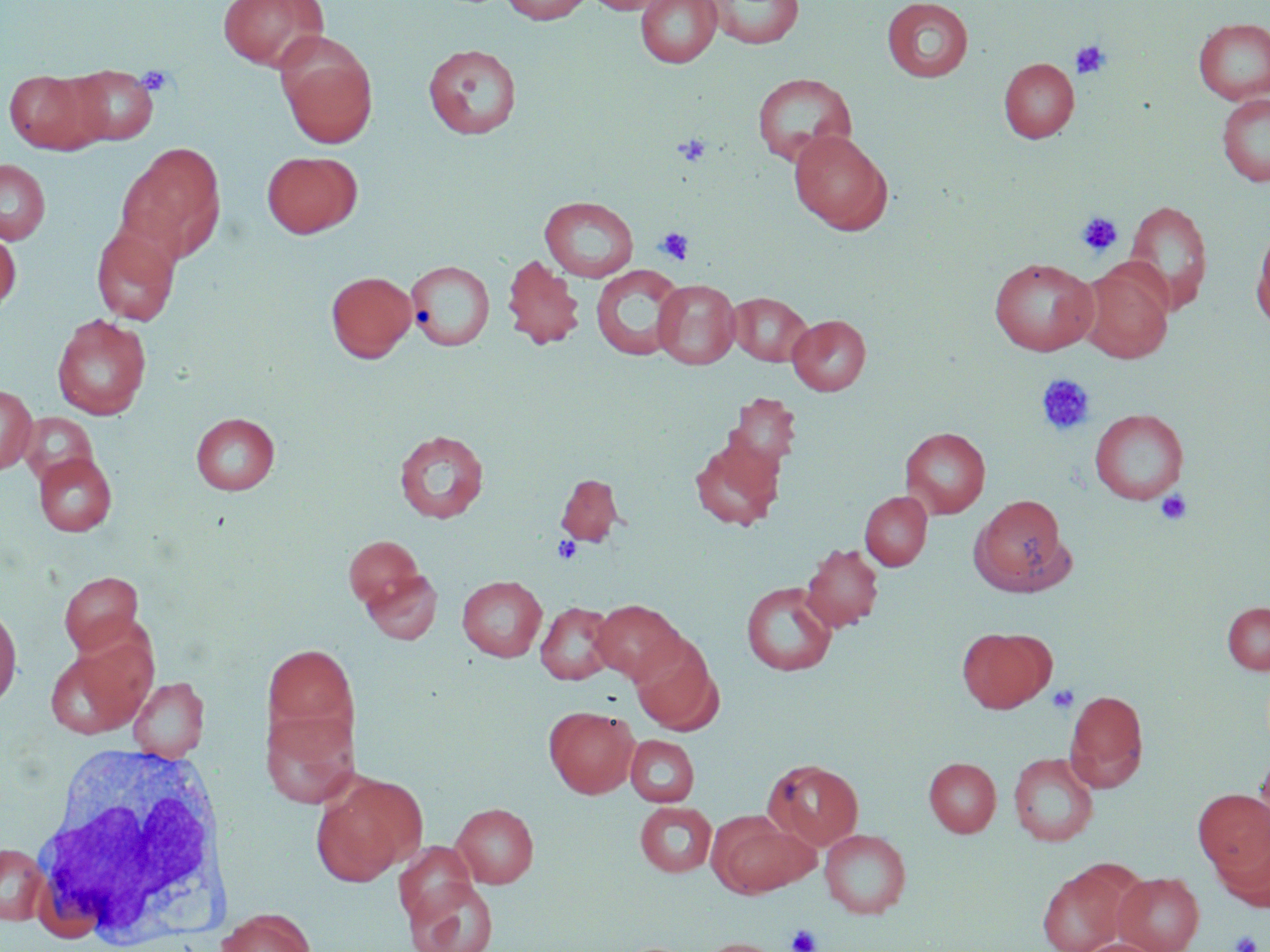
slide-level diagnosis = negative for blood parasites
image size = 1270×952 pixels
modality = light microscopy
platelet locations = approximate bounding boxes as named x1/y1/x2/y2 corners in pixels: (x1=1070, y1=40, x2=1112, y2=80), (x1=137, y1=65, x2=177, y2=97), (x1=673, y1=134, x2=711, y2=166), (x1=1076, y1=211, x2=1123, y2=257), (x1=655, y1=226, x2=694, y2=266), (x1=1036, y1=374, x2=1096, y2=436), (x1=1155, y1=490, x2=1193, y2=525), (x1=552, y1=536, x2=582, y2=564), (x1=1047, y1=684, x2=1079, y2=713), (x1=786, y1=924, x2=822, y2=952), (x1=1230, y1=931, x2=1262, y2=952)
stain = May-Grünwald-Giemsa
white blood cell locations = approximate bounding boxes as named x1/y1/x2/y2 corners in pixels: (x1=24, y1=743, x2=230, y2=951)
preparation = thin blood film
uninfected red blood cell locations = approximate bounding boxes as named x1/y1/x2/y2 corners in pixels: (x1=217, y1=0, x2=328, y2=72), (x1=500, y1=0, x2=592, y2=25), (x1=586, y1=0, x2=671, y2=14), (x1=635, y1=0, x2=722, y2=68), (x1=703, y1=0, x2=804, y2=49), (x1=881, y1=0, x2=973, y2=82), (x1=1193, y1=17, x2=1270, y2=105), (x1=275, y1=36, x2=378, y2=150), (x1=423, y1=43, x2=522, y2=139), (x1=999, y1=57, x2=1079, y2=143), (x1=63, y1=64, x2=160, y2=144), (x1=4, y1=69, x2=106, y2=154), (x1=751, y1=72, x2=858, y2=168), (x1=1216, y1=93, x2=1270, y2=187), (x1=789, y1=129, x2=893, y2=233), (x1=115, y1=141, x2=226, y2=264), (x1=262, y1=150, x2=362, y2=238), (x1=0, y1=158, x2=51, y2=244), (x1=540, y1=196, x2=639, y2=282), (x1=1123, y1=199, x2=1213, y2=313), (x1=1251, y1=222, x2=1270, y2=332), (x1=91, y1=225, x2=181, y2=326), (x1=0, y1=228, x2=21, y2=315), (x1=502, y1=254, x2=585, y2=350), (x1=989, y1=257, x2=1098, y2=356), (x1=405, y1=259, x2=494, y2=352), (x1=1078, y1=262, x2=1174, y2=362), (x1=590, y1=264, x2=686, y2=360), (x1=326, y1=270, x2=417, y2=362), (x1=652, y1=278, x2=740, y2=369), (x1=727, y1=292, x2=813, y2=366), (x1=51, y1=314, x2=152, y2=420), (x1=788, y1=314, x2=871, y2=395), (x1=0, y1=384, x2=37, y2=473), (x1=725, y1=393, x2=802, y2=474), (x1=1089, y1=408, x2=1189, y2=505), (x1=191, y1=412, x2=280, y2=495), (x1=20, y1=413, x2=97, y2=487), (x1=900, y1=426, x2=991, y2=517), (x1=394, y1=429, x2=489, y2=523), (x1=689, y1=436, x2=784, y2=531), (x1=34, y1=452, x2=118, y2=536), (x1=555, y1=473, x2=624, y2=546), (x1=860, y1=491, x2=932, y2=571), (x1=971, y1=494, x2=1072, y2=595), (x1=343, y1=535, x2=427, y2=612), (x1=801, y1=544, x2=884, y2=632), (x1=360, y1=566, x2=442, y2=645), (x1=59, y1=571, x2=144, y2=656), (x1=457, y1=575, x2=547, y2=661), (x1=741, y1=580, x2=837, y2=676), (x1=591, y1=599, x2=686, y2=684), (x1=0, y1=601, x2=22, y2=710), (x1=1221, y1=601, x2=1270, y2=675), (x1=535, y1=602, x2=618, y2=685), (x1=957, y1=627, x2=1054, y2=713), (x1=630, y1=633, x2=721, y2=734), (x1=263, y1=642, x2=359, y2=745), (x1=44, y1=643, x2=152, y2=738), (x1=128, y1=676, x2=209, y2=759), (x1=1065, y1=689, x2=1149, y2=791), (x1=260, y1=706, x2=360, y2=808), (x1=544, y1=706, x2=639, y2=798), (x1=626, y1=735, x2=699, y2=807), (x1=1254, y1=750, x2=1270, y2=851), (x1=1008, y1=752, x2=1099, y2=846), (x1=924, y1=757, x2=1001, y2=837), (x1=763, y1=758, x2=864, y2=852), (x1=312, y1=774, x2=425, y2=883), (x1=1193, y1=790, x2=1270, y2=881), (x1=635, y1=801, x2=717, y2=877), (x1=451, y1=802, x2=539, y2=888), (x1=710, y1=815, x2=815, y2=897), (x1=1212, y1=826, x2=1270, y2=912), (x1=819, y1=828, x2=911, y2=918), (x1=0, y1=842, x2=50, y2=923), (x1=393, y1=843, x2=480, y2=926), (x1=1037, y1=863, x2=1134, y2=952), (x1=1113, y1=871, x2=1204, y2=952), (x1=404, y1=877, x2=497, y2=952), (x1=216, y1=907, x2=316, y2=952), (x1=697, y1=938, x2=783, y2=952), (x1=1077, y1=938, x2=1165, y2=952)
field of view = one of a larger specimen
magnification = 1000x